Locate every Plasmodium falciparum-infected red blood cell.
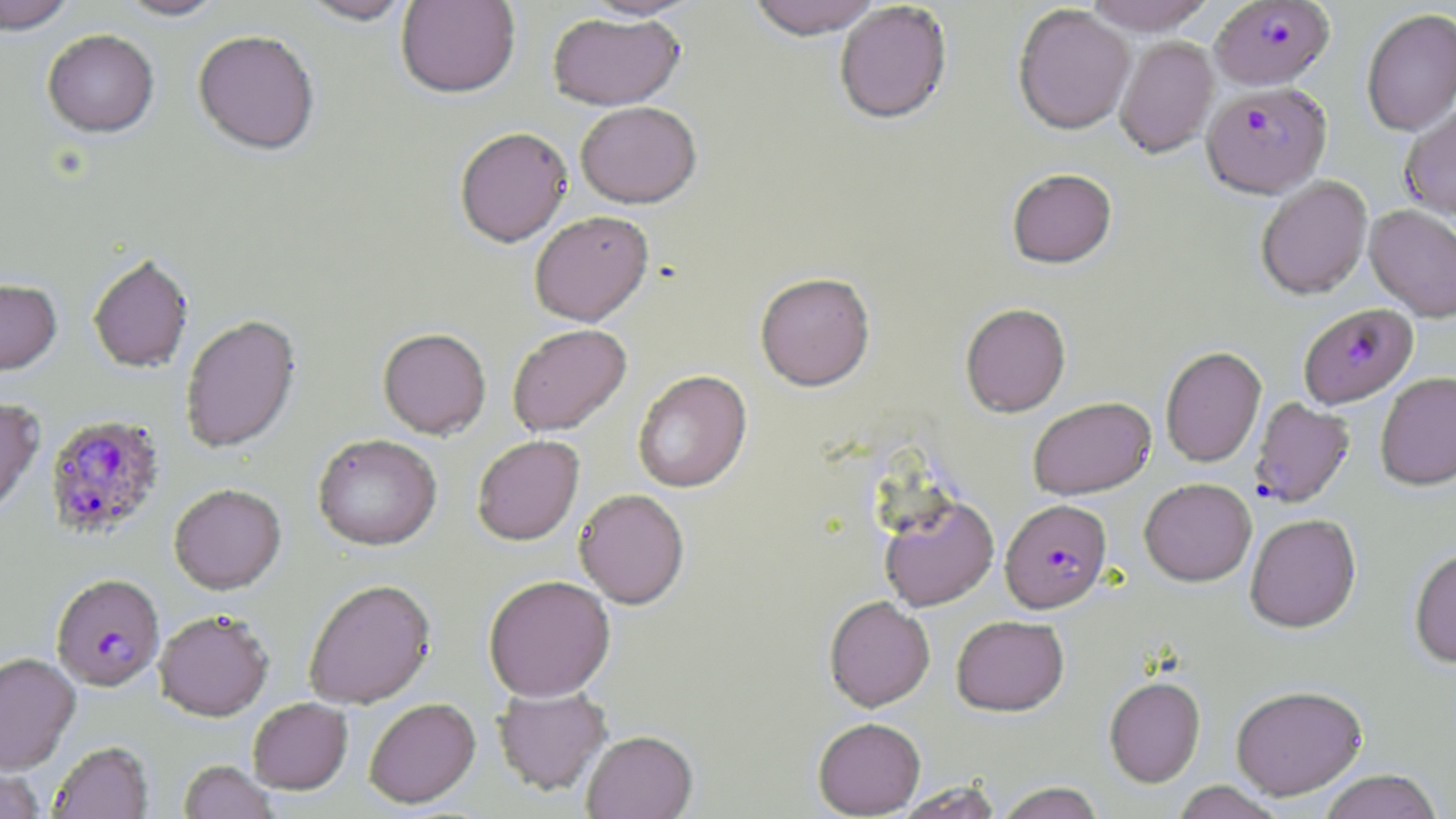
Approximate bounding boxes as named x1/y1/x2/y2 corners in pixels.
Plasmodium falciparum-infected red blood cells: (x1=1211, y1=1, x2=1334, y2=91), (x1=1202, y1=83, x2=1331, y2=198), (x1=1299, y1=302, x2=1418, y2=409), (x1=1250, y1=397, x2=1355, y2=508), (x1=45, y1=414, x2=165, y2=540), (x1=1000, y1=498, x2=1111, y2=612), (x1=51, y1=573, x2=164, y2=691).

Summary:
  - Uninfected red blood cell locations: (x1=0, y1=0, x2=76, y2=35), (x1=115, y1=0, x2=227, y2=21), (x1=297, y1=0, x2=415, y2=25), (x1=395, y1=0, x2=521, y2=98), (x1=581, y1=0, x2=701, y2=21), (x1=747, y1=0, x2=883, y2=40), (x1=1082, y1=0, x2=1217, y2=36), (x1=835, y1=2, x2=952, y2=125), (x1=1013, y1=5, x2=1136, y2=135), (x1=1361, y1=7, x2=1456, y2=137), (x1=547, y1=13, x2=685, y2=111), (x1=43, y1=29, x2=159, y2=138), (x1=193, y1=29, x2=320, y2=155), (x1=1115, y1=36, x2=1218, y2=158), (x1=575, y1=101, x2=701, y2=208), (x1=1401, y1=105, x2=1456, y2=220), (x1=454, y1=127, x2=572, y2=247), (x1=1006, y1=168, x2=1117, y2=269), (x1=1256, y1=175, x2=1372, y2=299), (x1=1365, y1=205, x2=1456, y2=322), (x1=529, y1=210, x2=653, y2=326), (x1=87, y1=253, x2=194, y2=373), (x1=755, y1=272, x2=875, y2=391), (x1=0, y1=278, x2=62, y2=376), (x1=960, y1=302, x2=1071, y2=417), (x1=180, y1=314, x2=301, y2=454), (x1=507, y1=323, x2=632, y2=436), (x1=378, y1=327, x2=491, y2=439), (x1=1160, y1=346, x2=1266, y2=467), (x1=632, y1=370, x2=751, y2=493), (x1=1375, y1=372, x2=1456, y2=491), (x1=1027, y1=396, x2=1155, y2=499), (x1=0, y1=397, x2=45, y2=520), (x1=312, y1=433, x2=442, y2=551), (x1=472, y1=435, x2=584, y2=545), (x1=1139, y1=478, x2=1256, y2=586), (x1=169, y1=483, x2=287, y2=595), (x1=574, y1=489, x2=689, y2=608), (x1=879, y1=494, x2=999, y2=611), (x1=1245, y1=513, x2=1361, y2=632), (x1=1409, y1=547, x2=1456, y2=668), (x1=483, y1=574, x2=616, y2=702), (x1=303, y1=578, x2=437, y2=708), (x1=824, y1=596, x2=935, y2=711), (x1=154, y1=609, x2=274, y2=721), (x1=952, y1=615, x2=1069, y2=715), (x1=0, y1=651, x2=81, y2=775), (x1=1104, y1=676, x2=1205, y2=787), (x1=1230, y1=684, x2=1366, y2=799), (x1=493, y1=685, x2=612, y2=795), (x1=364, y1=697, x2=481, y2=808), (x1=248, y1=698, x2=353, y2=795), (x1=812, y1=717, x2=925, y2=817), (x1=582, y1=729, x2=698, y2=819), (x1=49, y1=741, x2=153, y2=819), (x1=179, y1=760, x2=279, y2=819), (x1=1, y1=766, x2=46, y2=818), (x1=1317, y1=769, x2=1443, y2=819), (x1=893, y1=781, x2=1003, y2=818), (x1=1170, y1=781, x2=1286, y2=818), (x1=993, y1=782, x2=1108, y2=819)
  - Slide-level diagnosis: Plasmodium falciparum
  - Modality: light microscopy
  - Image size: 1456×819 pixels
  - Field of view: single
  - Preparation: thin blood smear
  - Magnification: 1000x
  - Stain: May-Grünwald-Giemsa